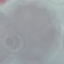

result = no malaria parasites detected
preparation = thin blood smear
capture = smartphone camera at the microscope eyepiece
stain = Giemsa
image type = automatically extracted cell patch, resized to 64 × 64 pixels